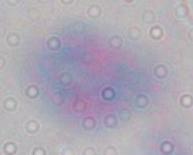
Toxoplasma gondii is seen. Captured at 1000x magnification. Photomicrograph.